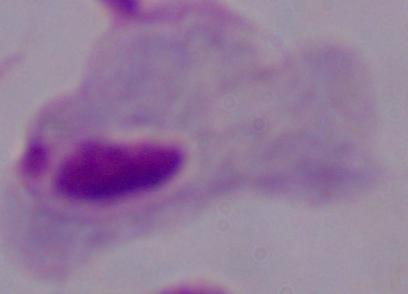
modality = micrograph
identification = trichomonad
magnification = 1000x